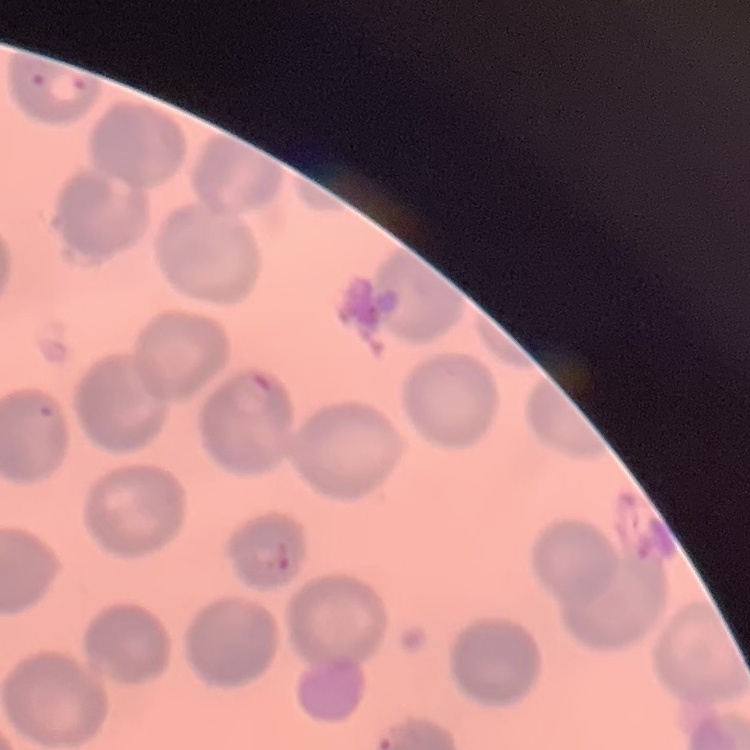

The erythrocytes show no rouleaux formation. Thin blood smear. Field's or Giemsa stain. One tile cut from a larger photomicrograph.